Assess this cell for malaria.
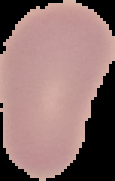
Uninfected.

Image is 115×181 pixels. The area outside the segmented cell region is set to black. From a thin blood film.